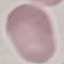 Result: negative for malaria parasites. Thin blood film. Giemsa stain. Cell patch, automatically extracted from a larger field of view and resized to 64 × 64 pixels. Acquired by smartphone through the microscope eyepiece.